Assess this cell for malaria.
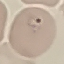
Parasitized.

image type = automatically extracted cell patch, resized to 64 × 64 pixels
stain = Giemsa
capture = smartphone camera at the microscope eyepiece
preparation = thin blood smear